State the blood parasite species.
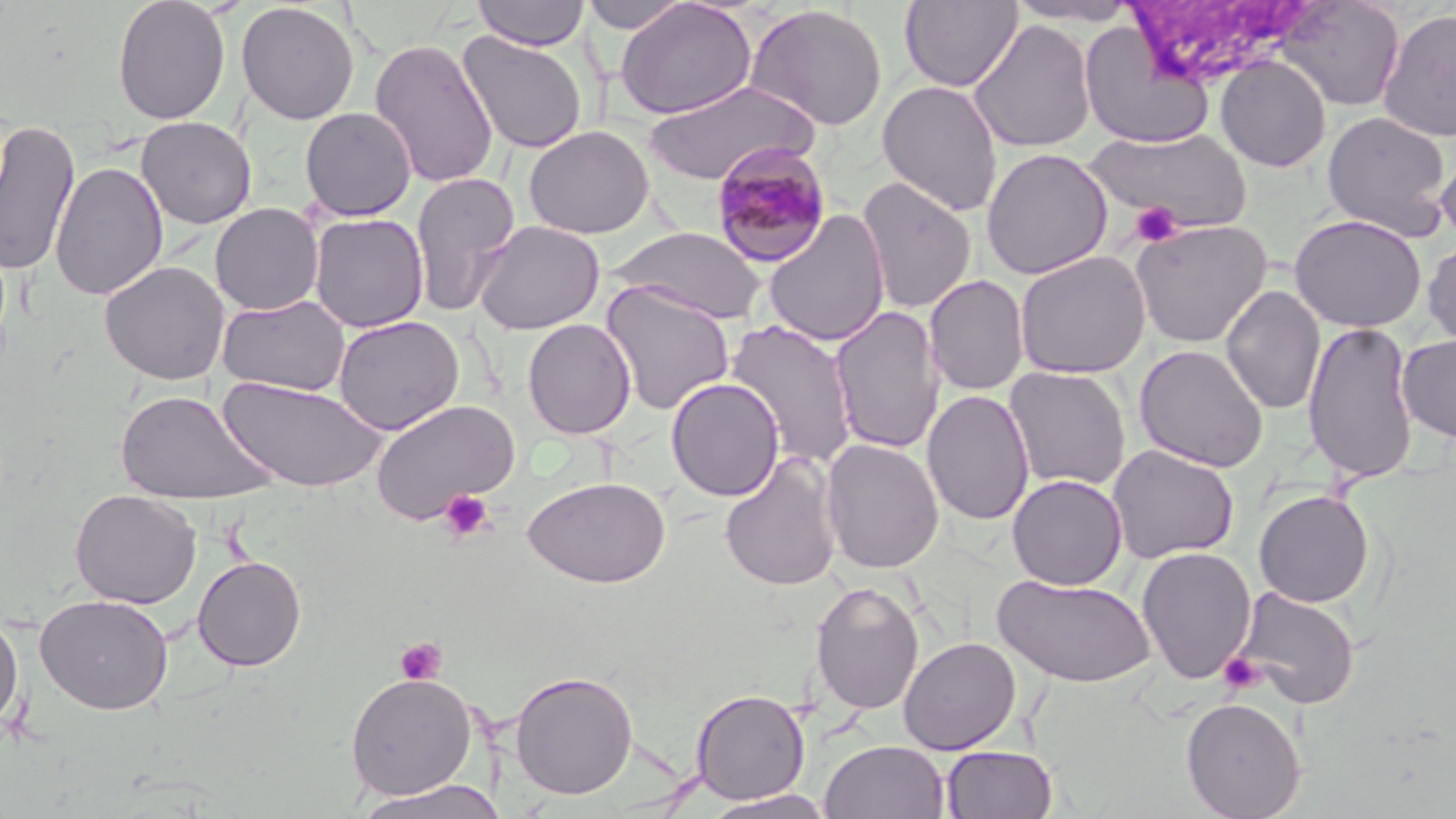

Plasmodium malariae.

Summary:
  - Coordinate format: approximate bounding boxes as (x1,y1)-(x2,y2) corner pairs in pixels
  - Uninfected red blood cell locations: (112,0)-(231,125), (471,0)-(590,51), (579,0)-(692,33), (616,0)-(757,120), (899,0)-(1022,92), (1004,0)-(1144,26), (1274,0)-(1405,112), (236,1)-(360,125), (745,4)-(888,132), (1377,8)-(1456,142), (969,20)-(1096,153), (1079,23)-(1215,149), (457,31)-(588,154), (368,37)-(499,188), (1214,55)-(1331,172), (643,80)-(817,186), (877,80)-(1003,217), (300,107)-(418,221), (1321,111)-(1452,240), (136,116)-(256,229), (0,118)-(80,278), (523,125)-(654,239), (1087,127)-(1252,232), (1435,143)-(1456,245), (981,147)-(1114,279), (50,161)-(168,301), (410,172)-(521,317), (857,177)-(977,315), (210,203)-(324,316), (763,211)-(890,347), (309,213)-(429,332), (1290,214)-(1427,332), (1130,219)-(1272,347), (473,220)-(605,335), (608,226)-(767,324), (1423,236)-(1456,350), (1015,251)-(1151,378), (99,261)-(230,385), (924,274)-(1029,396), (601,281)-(735,416), (1221,284)-(1325,416), (217,294)-(350,397), (830,305)-(945,455), (334,316)-(464,435), (522,318)-(636,440), (725,319)-(860,470), (1302,319)-(1420,486), (1397,334)-(1456,443), (1134,343)-(1270,472), (1003,366)-(1131,492), (218,376)-(389,492), (665,377)-(785,502), (115,388)-(281,506), (922,389)-(1035,526), (371,399)-(520,524), (821,439)-(944,574), (1106,443)-(1240,564), (718,451)-(843,592), (1007,474)-(1127,590), (522,475)-(672,588), (70,489)-(201,609), (1254,489)-(1375,608), (1136,547)-(1257,684), (192,555)-(307,671), (994,573)-(1156,688), (809,579)-(926,717), (1233,586)-(1361,710), (35,593)-(174,714), (0,610)-(23,733), (898,636)-(1021,755), (511,670)-(639,799), (346,673)-(479,800), (690,687)-(811,804), (1180,696)-(1307,819), (820,739)-(950,819), (942,745)-(1059,818), (355,779)-(504,819), (703,790)-(835,818)
  - Platelet locations: (1131,201)-(1182,247), (437,489)-(495,543), (395,638)-(447,685), (1219,652)-(1265,694)
  - Plasmodium malariae-infected red blood cell locations: (710,142)-(833,267)
  - Stain: May-Grünwald-Giemsa
  - Magnification: 1000x
  - Preparation: thin blood smear
  - Field of view: one of a larger specimen
  - Image size: 1456×819 pixels
  - Modality: light microscopy